Point out each Plasmodium parasite.
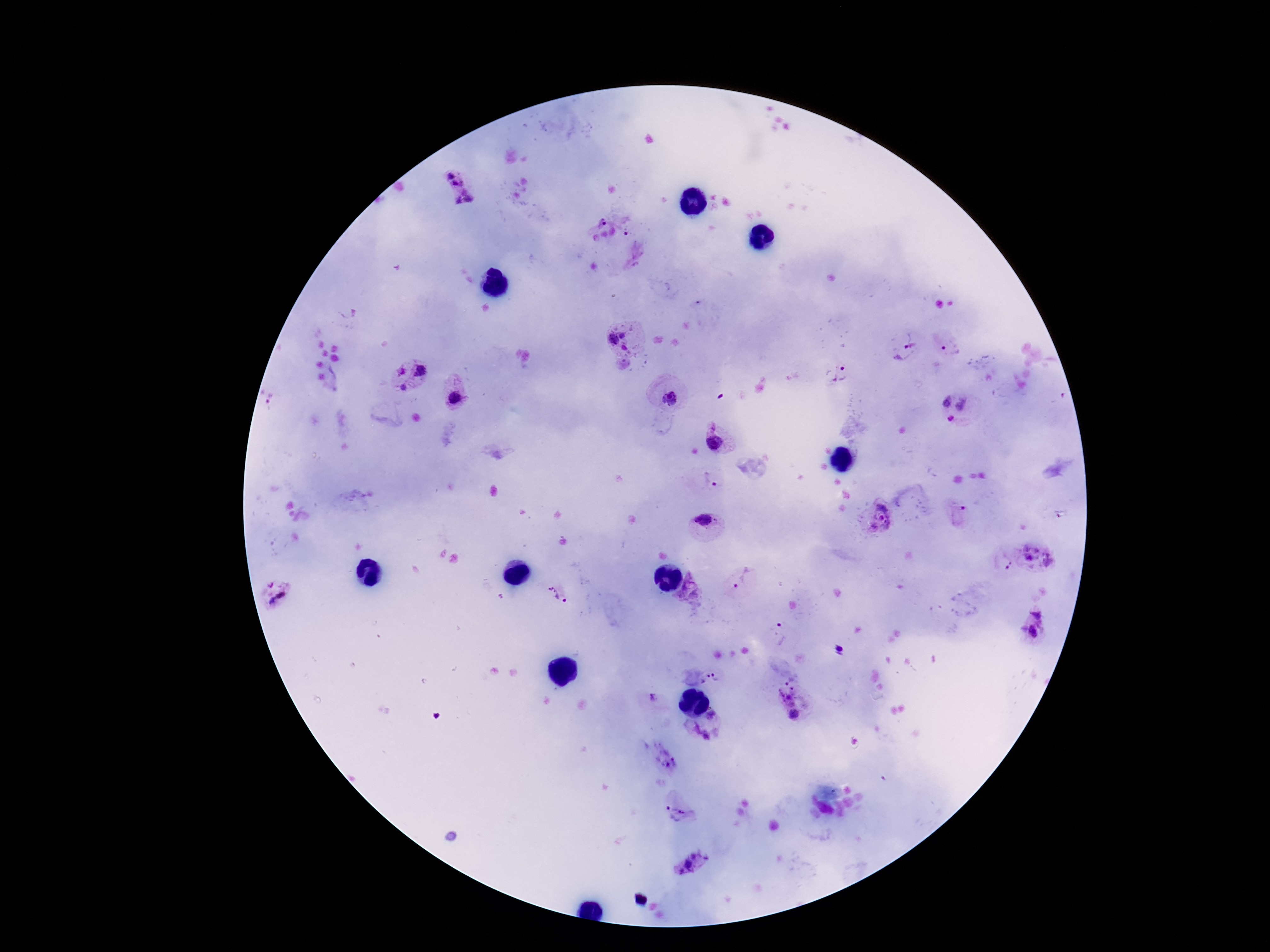
Approximate centers as {x, y} in pixels.
Plasmodium parasites: {450, 175}, {457, 183}, {470, 200}, {458, 201}, {600, 221}, {630, 230}, {624, 335}, {613, 340}, {625, 348}, {903, 348}, {952, 348}, {400, 370}, {420, 370}, {843, 372}, {404, 387}, {455, 398}, {671, 400}, {944, 402}, {965, 406}, {951, 419}, {714, 442}, {708, 483}, {961, 509}, {880, 519}, {703, 520}, {1039, 556}, {1007, 562}, {741, 580}, {270, 584}, {560, 594}, {281, 595}, {272, 601}, {1040, 610}, {779, 634}, {1033, 634}, {710, 679}, {787, 692}, {794, 714}, {713, 715}, {708, 735}, {666, 758}, {678, 814}, {695, 857}, {689, 864}, {679, 871}.

patient malaria status = infected
stain = Giemsa
preparation = thick blood smear
capture = smartphone camera through the microscope eyepiece
field of view = single
magnification = 100x
image size = 1270×952 pixels